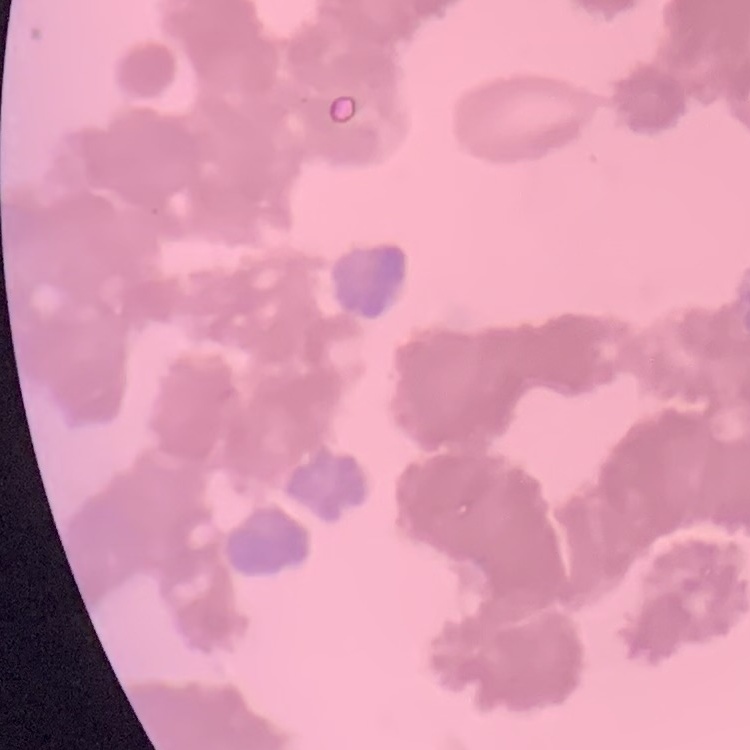

red blood cell morphology = rouleaux formation
image type = square crop of a larger photomicrograph
stain = Field's or Giemsa
preparation = thin blood film